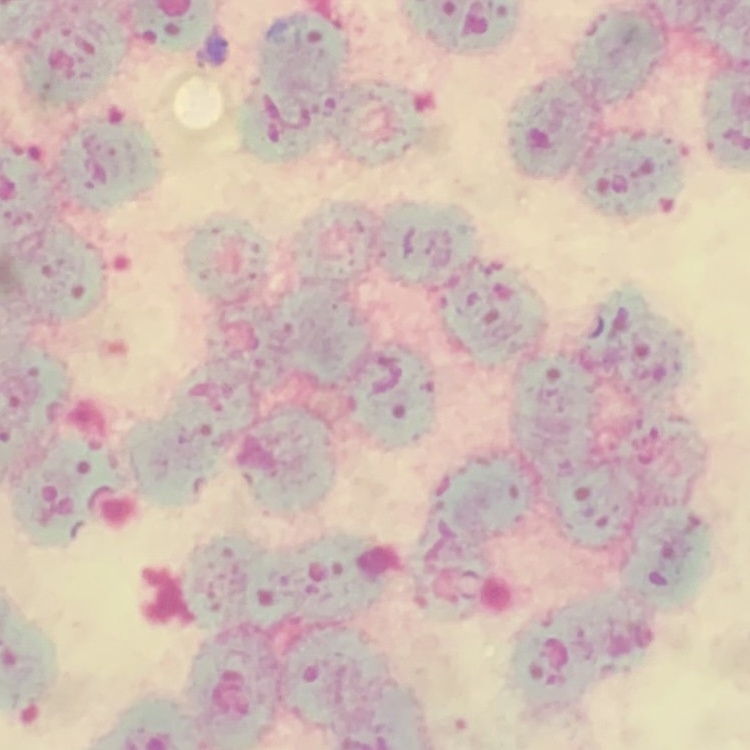
red blood cell morphology = rouleaux formation
preparation = thin blood film
stain = Field's or Giemsa
image type = one tile cut from a larger photomicrograph